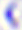
magnification = 400x
identification = Toxoplasma gondii
modality = photomicrograph